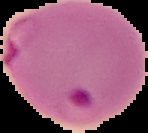 Segmented cell region on a black background. Image is 148×133 pixels. Malaria status: parasitized. From a thin blood smear.